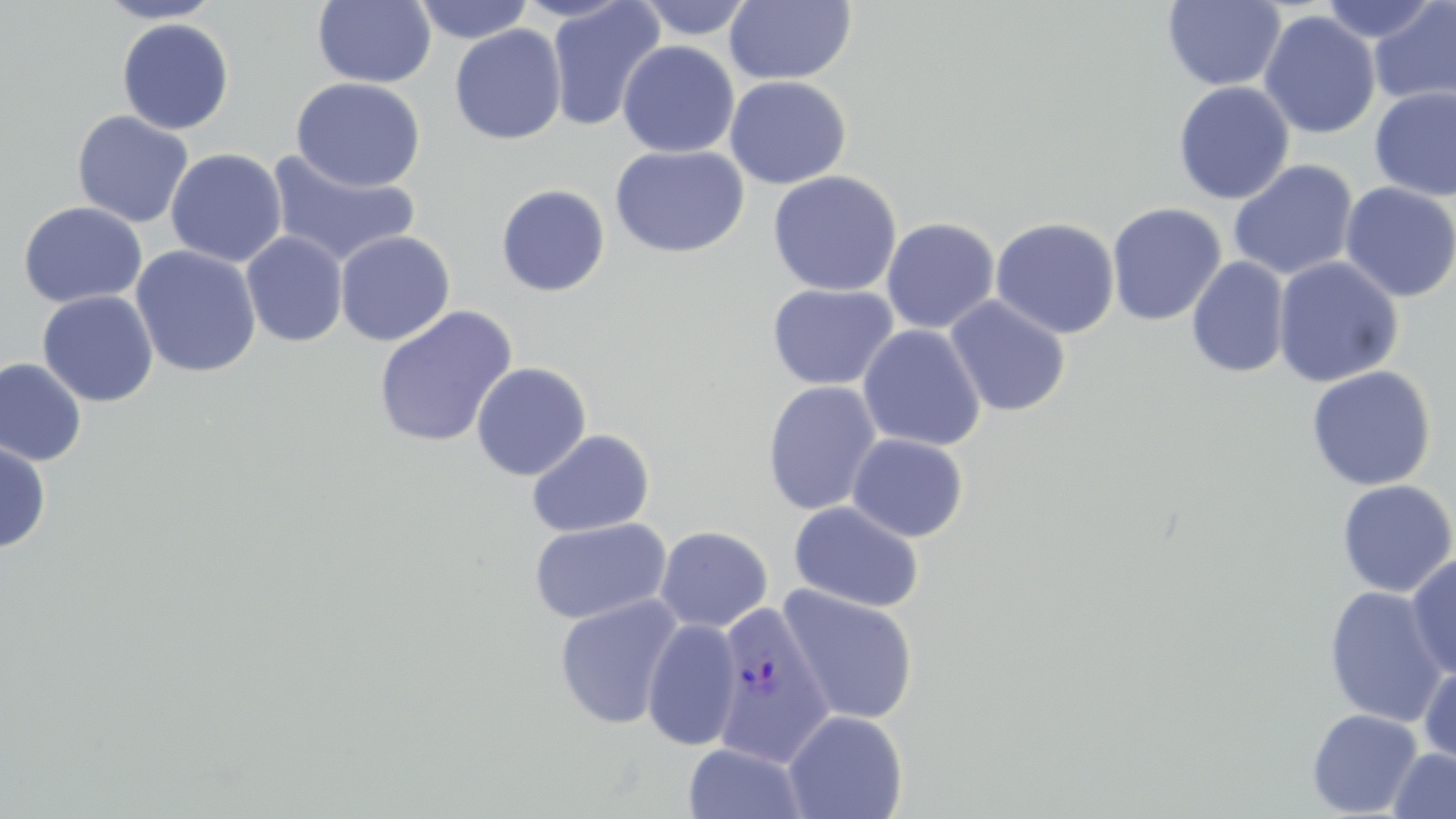 Approximate bounding boxes as named x1/y1/x2/y2 corners in pixels. Uninfected red blood cell locations: (x1=96, y1=0, x2=224, y2=24), (x1=412, y1=0, x2=534, y2=44), (x1=546, y1=0, x2=666, y2=133), (x1=634, y1=0, x2=757, y2=40), (x1=1163, y1=0, x2=1286, y2=91), (x1=1315, y1=0, x2=1441, y2=45), (x1=1369, y1=0, x2=1456, y2=111), (x1=312, y1=1, x2=437, y2=88), (x1=724, y1=1, x2=857, y2=86), (x1=1258, y1=11, x2=1381, y2=139), (x1=116, y1=18, x2=235, y2=135), (x1=448, y1=24, x2=567, y2=145), (x1=616, y1=41, x2=740, y2=159), (x1=724, y1=75, x2=851, y2=189), (x1=290, y1=77, x2=427, y2=191), (x1=1173, y1=80, x2=1295, y2=205), (x1=1369, y1=86, x2=1456, y2=201), (x1=71, y1=110, x2=194, y2=228), (x1=610, y1=145, x2=749, y2=258), (x1=165, y1=148, x2=288, y2=267), (x1=265, y1=150, x2=422, y2=270), (x1=1228, y1=159, x2=1359, y2=281), (x1=767, y1=170, x2=903, y2=297), (x1=1339, y1=181, x2=1455, y2=302), (x1=495, y1=184, x2=610, y2=297), (x1=17, y1=201, x2=148, y2=308), (x1=1106, y1=202, x2=1227, y2=326), (x1=990, y1=216, x2=1120, y2=339), (x1=880, y1=217, x2=1000, y2=334), (x1=241, y1=230, x2=349, y2=347), (x1=335, y1=230, x2=456, y2=346), (x1=130, y1=245, x2=262, y2=379), (x1=1186, y1=256, x2=1290, y2=379), (x1=1272, y1=256, x2=1404, y2=388), (x1=766, y1=282, x2=899, y2=391), (x1=37, y1=290, x2=158, y2=407), (x1=944, y1=296, x2=1071, y2=417), (x1=372, y1=305, x2=518, y2=449), (x1=857, y1=324, x2=986, y2=452), (x1=0, y1=358, x2=87, y2=467), (x1=470, y1=362, x2=592, y2=481), (x1=1305, y1=365, x2=1436, y2=492), (x1=762, y1=380, x2=882, y2=516), (x1=526, y1=429, x2=655, y2=537), (x1=847, y1=434, x2=968, y2=542), (x1=0, y1=439, x2=52, y2=554), (x1=1335, y1=479, x2=1456, y2=598), (x1=788, y1=500, x2=925, y2=613), (x1=528, y1=518, x2=671, y2=625), (x1=655, y1=526, x2=773, y2=633), (x1=1405, y1=552, x2=1456, y2=679), (x1=777, y1=584, x2=920, y2=725), (x1=1323, y1=586, x2=1450, y2=727), (x1=553, y1=594, x2=685, y2=730), (x1=642, y1=617, x2=743, y2=752), (x1=1418, y1=662, x2=1456, y2=770), (x1=1306, y1=708, x2=1422, y2=817), (x1=783, y1=709, x2=909, y2=819), (x1=683, y1=742, x2=809, y2=818), (x1=1387, y1=747, x2=1456, y2=818). Plasmodium vivax-infected red blood cell locations: (x1=704, y1=606, x2=835, y2=763). Slide-level diagnosis: Plasmodium vivax. Thin blood smear. May-Grünwald-Giemsa-stained preparation. Image is 1456×819 pixels. Single field of view. 1000x magnification. Optical microscopy.